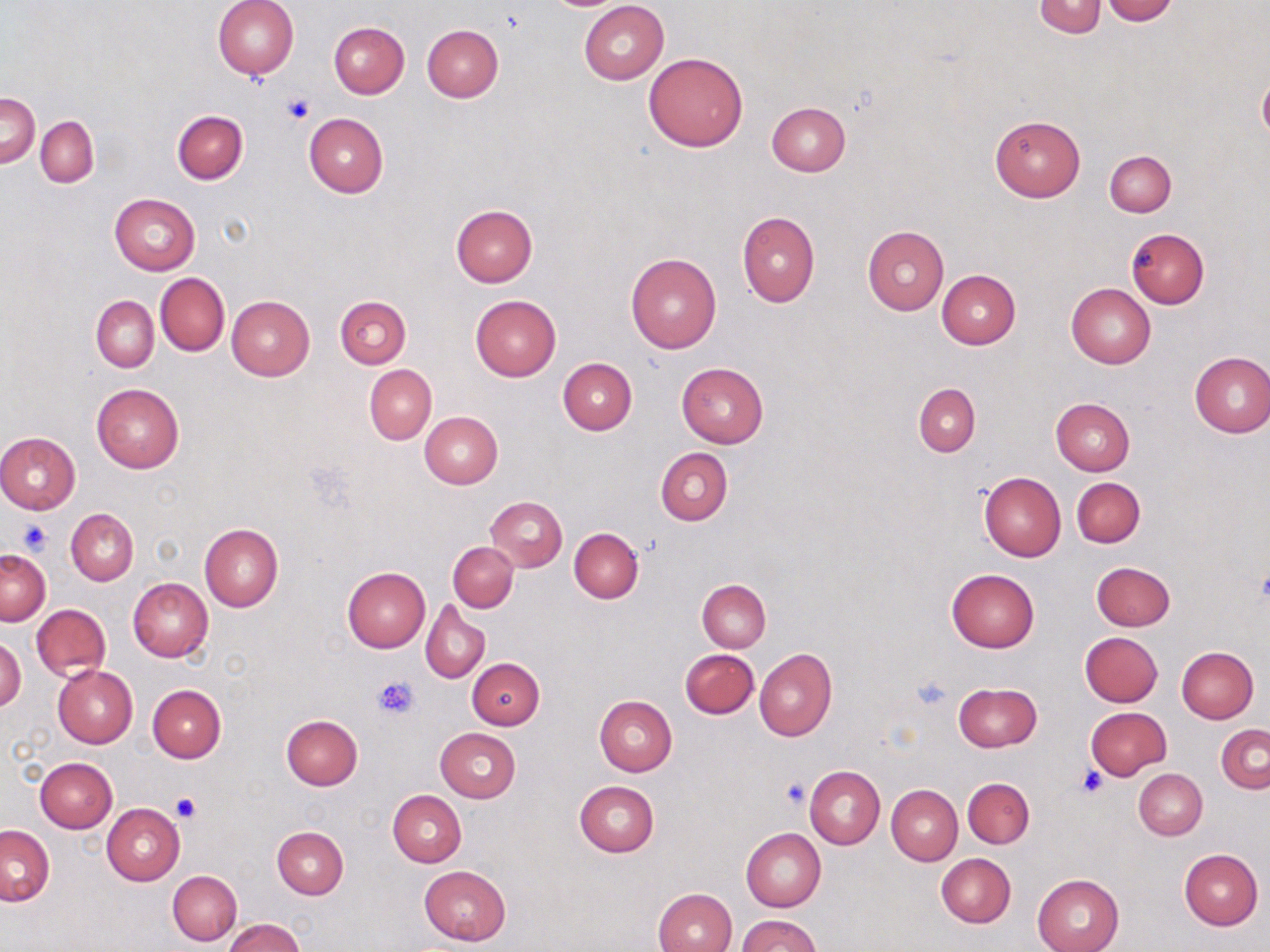
slide-level diagnosis = negative for blood parasites
stain = May-Grünwald-Giemsa
preparation = thin blood smear
modality = light microscopy
image size = 1270×952 pixels
magnification = 1000x
field of view = one of a larger specimen
uninfected red blood cell locations = approximate bounding boxes as (x1,y1)-(x2,y2) corner pairs in pixels: (214,0)-(299,78), (1101,0)-(1177,24), (578,1)-(668,85), (1033,1)-(1107,38), (329,22)-(410,98), (423,24)-(504,102), (643,52)-(749,151), (1,94)-(40,167), (767,102)-(850,176), (173,111)-(248,184), (304,114)-(387,197), (989,115)-(1084,202), (35,116)-(98,187), (1104,150)-(1175,217), (109,192)-(200,275), (450,205)-(538,287), (738,211)-(819,307), (862,226)-(949,314), (1127,228)-(1209,309), (625,252)-(721,354), (937,270)-(1021,348), (155,273)-(229,355), (1067,283)-(1155,368), (335,295)-(411,368), (470,295)-(561,381), (91,296)-(158,372), (226,296)-(315,380), (1189,351)-(1270,438), (558,357)-(637,435), (676,362)-(769,447), (365,365)-(437,443), (91,383)-(184,474), (913,383)-(980,456), (1050,398)-(1134,476), (420,411)-(503,488), (0,431)-(80,513), (656,448)-(733,525), (978,471)-(1066,562), (1072,478)-(1144,548), (487,497)-(567,571), (67,508)-(138,585), (199,524)-(283,611), (569,528)-(643,602), (448,542)-(517,612), (0,550)-(50,625), (1090,561)-(1175,631), (341,567)-(429,651), (946,567)-(1041,653), (128,578)-(213,663), (697,579)-(771,651), (421,600)-(490,682), (31,604)-(111,679), (1081,631)-(1162,706), (1,636)-(25,714), (1177,647)-(1258,724), (680,649)-(758,718), (754,649)-(836,741), (466,657)-(544,729), (54,665)-(138,747), (954,682)-(1042,752), (147,685)-(226,762), (594,695)-(677,776), (1085,707)-(1172,780), (280,714)-(362,789), (1216,723)-(1270,793), (436,728)-(519,803), (35,757)-(117,832), (805,766)-(885,849), (1134,769)-(1206,839), (963,778)-(1034,849), (574,781)-(658,857), (887,785)-(962,864), (388,790)-(466,867), (102,804)-(185,885), (1,825)-(54,905), (272,826)-(349,899), (741,827)-(826,911), (1179,848)-(1263,929), (935,854)-(1016,928), (418,866)-(510,946), (168,871)-(241,945), (1032,874)-(1124,952), (653,888)-(737,952), (737,915)-(821,952), (222,918)-(305,952)
platelet locations = approximate bounding boxes as (x1,y1)-(x2,y2) corner pairs in pixels: (282,91)-(315,125), (19,520)-(52,554), (372,673)-(419,720), (910,677)-(952,711), (1076,764)-(1109,797), (782,777)-(811,809), (173,792)-(201,821)